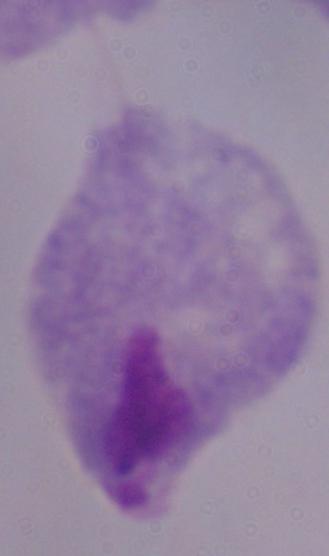

identification = trichomonad
magnification = 1000x
modality = photomicrograph